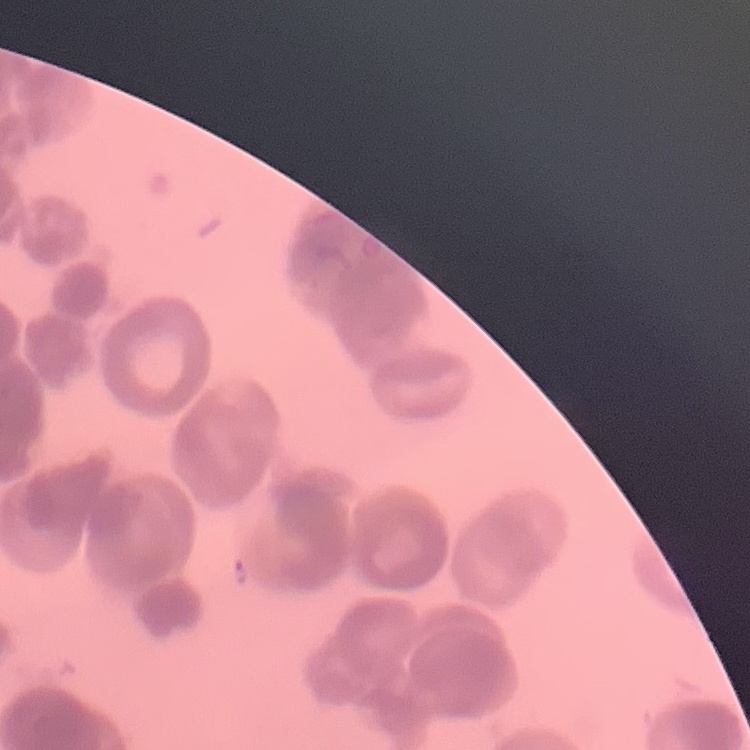
The erythrocytes exhibit rouleaux formation. Stained with either Field's or Giemsa. Thin peripheral smear. One tile cut from a larger photomicrograph.